Outline each blood parasite and name the species.
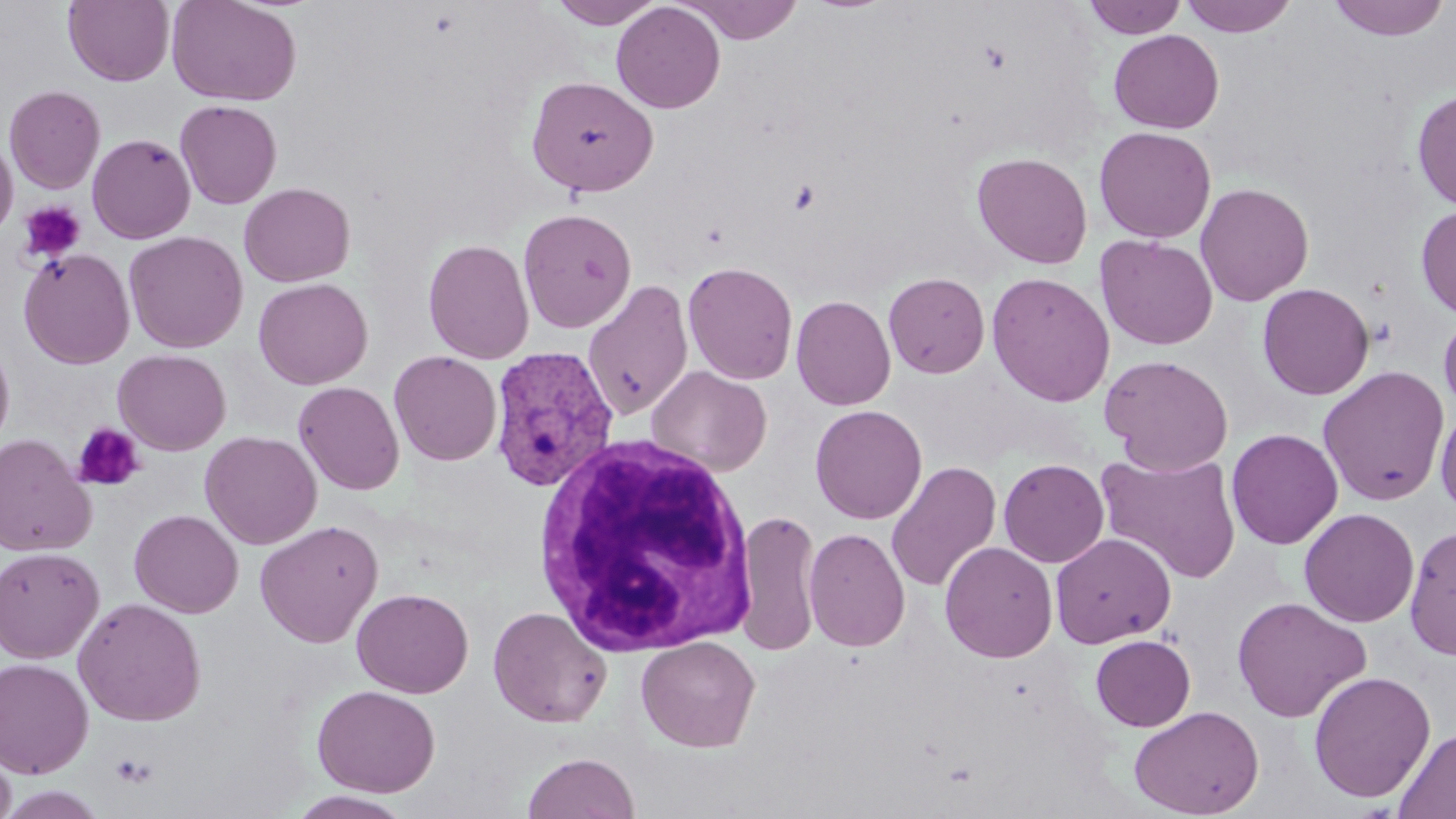

Approximate bounding boxes as (x1,y1)-(x2,y2) corner pairs in pixels.
Plasmodium vivax-infected red blood cells: (489,344)-(619,494).
No Plasmodium falciparum, Plasmodium ovale, Plasmodium malariae, Babesia divergens, or Trypanosoma brucei observed.

Summary:
  - Uninfected red blood cell locations: (63,0)-(174,86), (166,0)-(302,106), (549,0)-(665,29), (679,0)-(804,44), (1082,0)-(1187,39), (1178,0)-(1299,37), (1326,0)-(1452,42), (611,2)-(726,113), (1109,29)-(1225,134), (525,75)-(659,197), (4,85)-(106,194), (1411,88)-(1456,211), (174,100)-(283,209), (1094,126)-(1217,243), (87,133)-(196,244), (0,134)-(18,242), (971,151)-(1094,269), (239,181)-(355,287), (1194,182)-(1314,306), (1415,203)-(1456,322), (518,207)-(637,332), (124,231)-(248,353), (1095,235)-(1218,350), (422,239)-(535,364), (19,248)-(135,369), (682,261)-(798,385), (883,272)-(990,378), (986,272)-(1116,407), (252,277)-(373,389), (581,281)-(694,420), (1257,282)-(1374,400), (791,295)-(896,410), (1438,310)-(1456,419), (0,338)-(15,454), (113,349)-(231,455), (389,350)-(502,466), (1099,354)-(1234,474), (646,365)-(772,476), (1317,365)-(1450,506), (293,381)-(405,495), (1434,403)-(1456,519), (810,404)-(928,524), (1226,428)-(1343,549), (200,431)-(322,549), (0,434)-(97,557), (1095,449)-(1242,583), (998,458)-(1109,568), (885,461)-(1002,593), (1298,507)-(1420,628), (129,509)-(244,618), (734,509)-(822,657), (254,519)-(384,648), (1403,523)-(1455,660), (804,527)-(911,652), (1050,532)-(1176,648), (939,541)-(1058,663), (0,546)-(104,663), (352,588)-(474,698), (1232,595)-(1371,723), (72,597)-(207,726), (487,605)-(612,728), (1090,634)-(1196,731), (636,635)-(760,752), (0,658)-(94,777), (1308,670)-(1436,803), (312,684)-(440,797), (1129,704)-(1265,819), (1394,726)-(1456,818), (0,737)-(16,819), (522,752)-(640,819), (0,785)-(110,819), (288,791)-(416,818)
  - White blood cell locations: (532,432)-(758,656)
  - Platelet locations: (18,201)-(86,264), (72,422)-(146,492), (111,752)-(159,787)
  - Slide-level diagnosis: Plasmodium vivax
  - Magnification: 1000x
  - Modality: optical microscopy
  - Preparation: thin blood film
  - Stain: May-Grünwald-Giemsa
  - Image size: 1456×819 pixels
  - Field of view: one of a larger specimen